Locate every blood parasite and identify its species.
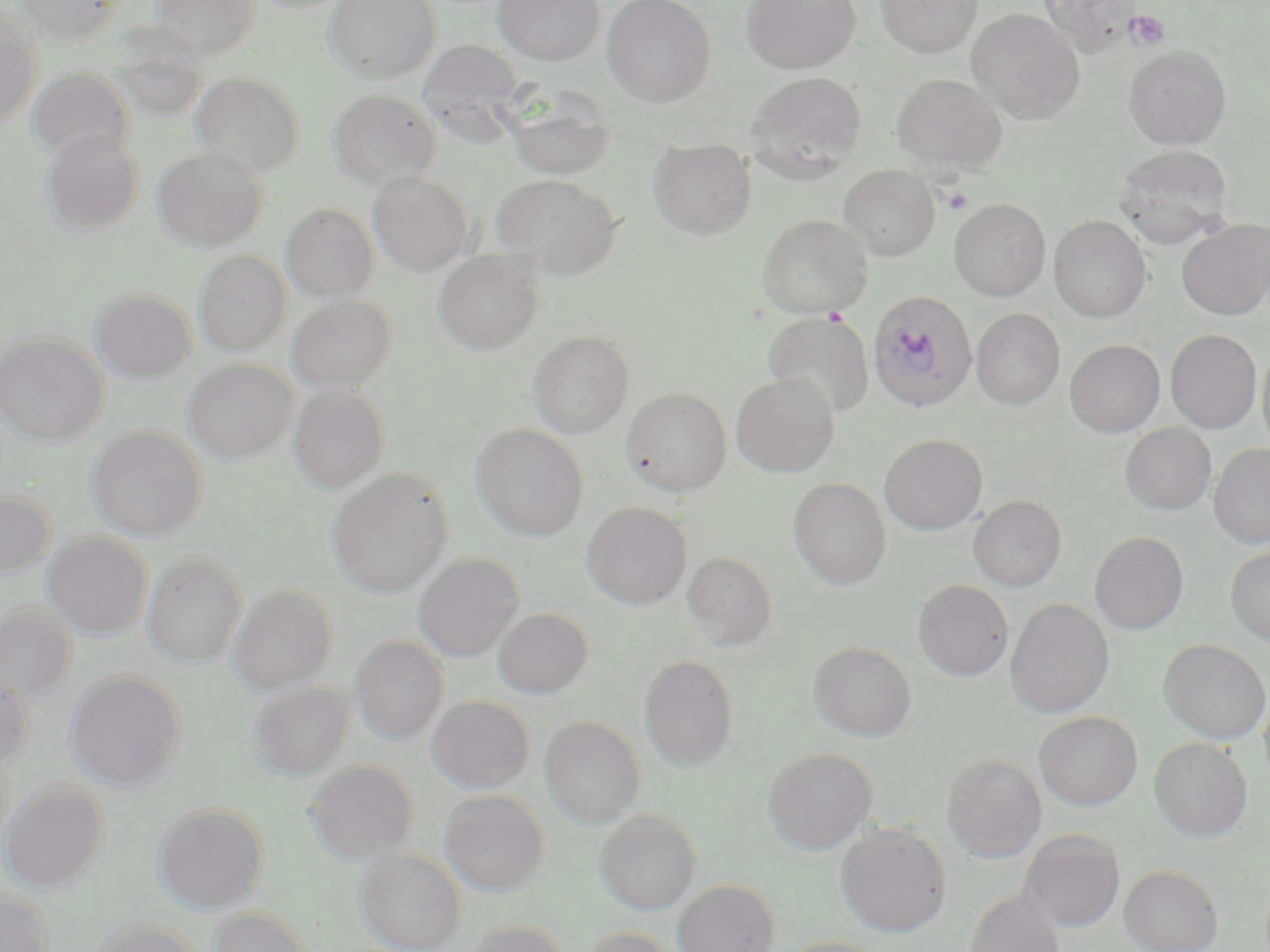
Approximate bounding boxes as (x1,y1)-(x2,y2) corner pairs in pixels.
Plasmodium falciparum-infected red blood cells: (868,290)-(978,412).
No Plasmodium ovale, Plasmodium malariae, Plasmodium vivax, Babesia divergens, or Trypanosoma brucei observed.

{
  "slide_level_diagnosis": "Plasmodium falciparum",
  "magnification": "1000x",
  "image_size": "1270×952 pixels",
  "preparation": "thin blood film",
  "uninfected_red_blood_cell_locations": "approximate bounding boxes as (x1,y1)-(x2,y2) corner pairs in pixels: (152,0)-(261,59), (323,0)-(439,83), (493,0)-(604,65), (603,0)-(716,105), (740,0)-(862,74), (875,0)-(982,58), (16,1)-(123,44), (1038,1)-(1142,54), (967,9)-(1085,124), (0,14)-(41,127), (411,41)-(537,152), (1124,45)-(1232,148), (28,68)-(133,163), (191,72)-(304,175), (746,72)-(867,178), (892,73)-(1007,174), (505,88)-(616,181), (328,89)-(440,191), (41,129)-(142,236), (650,139)-(755,239), (1114,145)-(1235,246), (152,148)-(264,250), (839,165)-(940,260), (369,173)-(472,275), (492,174)-(621,277), (949,199)-(1050,301), (281,204)-(377,303), (757,214)-(872,318), (1049,215)-(1151,322), (1177,219)-(1270,320), (433,250)-(543,354), (195,251)-(289,356), (92,287)-(194,384), (287,295)-(395,394), (972,308)-(1065,410), (764,312)-(873,418), (1166,329)-(1262,433), (528,331)-(634,437), (0,332)-(107,445), (1065,339)-(1165,437), (1257,345)-(1270,454), (184,360)-(297,462), (731,373)-(839,478), (288,385)-(388,494), (622,387)-(731,496), (1120,423)-(1216,515), (471,424)-(588,541), (87,426)-(206,540), (879,434)-(987,535), (1209,443)-(1270,547), (327,469)-(453,597), (788,477)-(891,590), (0,491)-(54,578), (968,495)-(1067,591), (582,502)-(691,609), (1090,531)-(1189,634), (43,532)-(151,639), (1225,546)-(1270,645), (143,551)-(246,667), (683,551)-(777,650), (414,553)-(523,661), (913,579)-(1013,681), (228,583)-(336,694), (1006,598)-(1114,718), (0,604)-(77,703), (492,608)-(592,699), (351,636)-(447,744), (1159,639)-(1269,743), (808,641)-(916,741), (639,654)-(739,771), (0,670)-(35,768), (66,670)-(185,790), (249,682)-(353,780), (1259,686)-(1270,791), (428,695)-(534,793), (1035,711)-(1142,810), (540,716)-(645,827), (1149,737)-(1253,842), (763,746)-(878,854), (942,753)-(1047,862), (305,759)-(418,863), (1,780)-(108,892), (441,790)-(549,896), (152,802)-(268,913), (594,809)-(700,914), (835,823)-(952,937), (1020,830)-(1125,932), (354,847)-(465,952), (1120,864)-(1223,952), (672,879)-(779,952), (965,887)-(1066,952), (0,890)-(54,952), (209,907)-(313,952), (90,917)-(204,952), (462,920)-(569,952), (579,927)-(679,952), (777,936)-(887,952)",
  "field_of_view": "one of a larger specimen",
  "modality": "light microscopy",
  "stain": "May-Grünwald-Giemsa",
  "platelet_locations": "approximate bounding boxes as (x1,y1)-(x2,y2) corner pairs in pixels: (1125,9)-(1170,50), (823,307)-(848,325)"
}